Assess this cell for malaria.
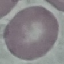

Uninfected.

Summary:
  - Image type: cell patch, automatically extracted from a larger field of view and resized to 64 × 64 pixels
  - Capture: smartphone through the microscope eyepiece
  - Stain: Giemsa
  - Preparation: thin blood smear